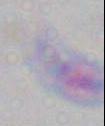

magnification: 1000x
modality: micrograph
identification: Toxoplasma gondii